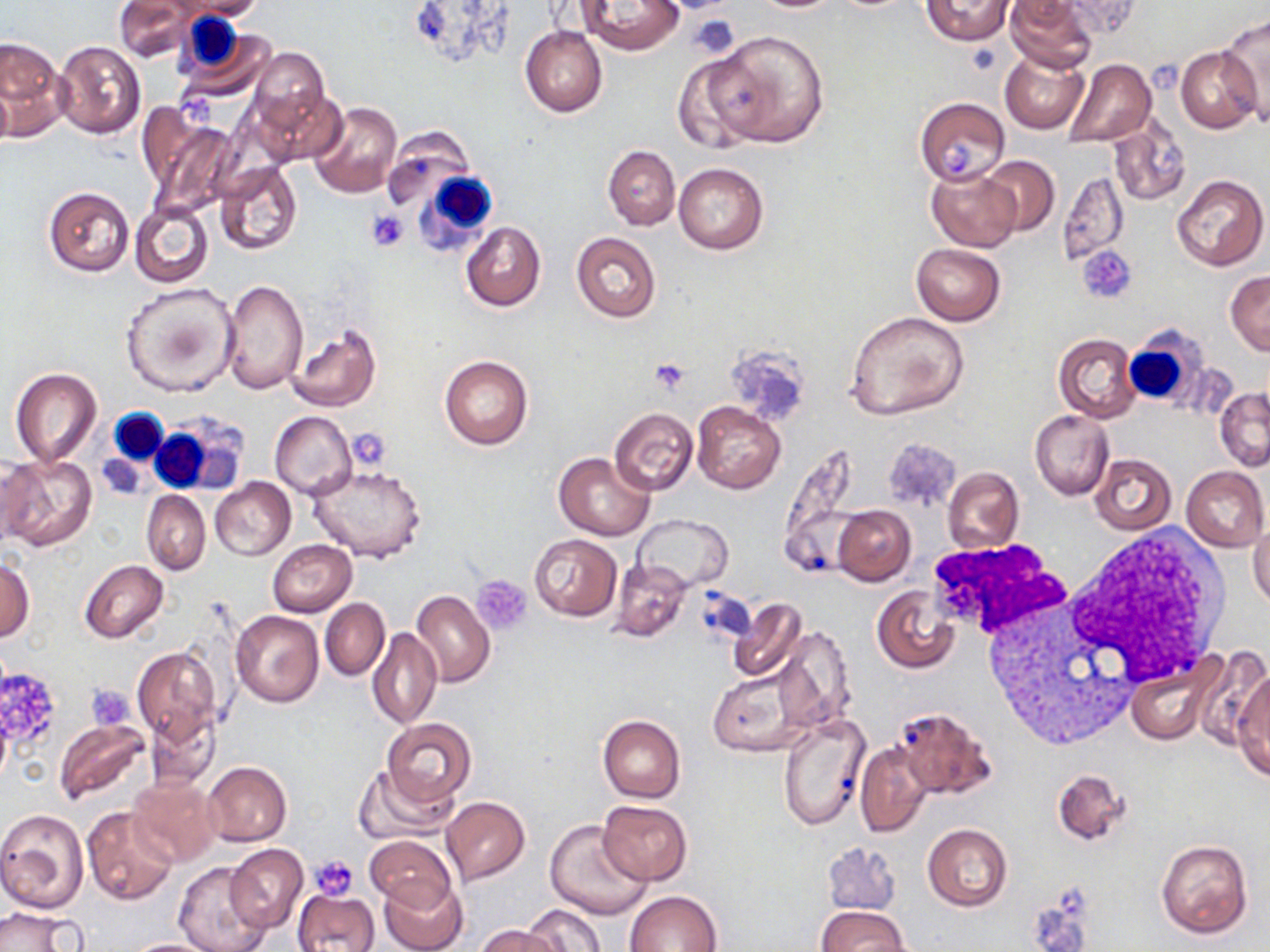 Approximate bounding boxes as (x1,y1)-(x2,y2) corner pairs in pixels. White blood cell locations: (175,10)-(245,77), (414,169)-(497,253), (1125,330)-(1205,409), (108,397)-(168,468), (151,413)-(245,499), (1064,528)-(1233,683), (934,549)-(1127,742). Platelet locations: (689,14)-(742,57), (1147,59)-(1178,93), (942,137)-(977,178), (367,210)-(409,252), (1079,247)-(1136,302), (650,358)-(693,394), (347,430)-(391,471), (473,575)-(532,635), (0,672)-(55,744), (85,683)-(135,731), (309,855)-(357,900). Uninfected red blood cell locations: (114,0)-(194,61), (169,0)-(266,21), (579,0)-(684,55), (920,0)-(1015,46), (1003,0)-(1097,74), (1057,0)-(1141,38), (1218,16)-(1270,125), (520,26)-(607,116), (179,27)-(277,104), (709,31)-(829,148), (1,36)-(67,139), (54,41)-(145,138), (1176,46)-(1262,133), (248,48)-(330,134), (1000,50)-(1087,135), (670,55)-(760,155), (1062,58)-(1155,147), (0,78)-(13,150), (255,86)-(346,167), (914,97)-(1011,185), (307,101)-(403,200), (142,108)-(238,214), (1109,118)-(1190,207), (379,127)-(477,216), (603,146)-(680,230), (979,154)-(1060,237), (214,160)-(302,256), (674,162)-(768,255), (925,165)-(1020,252), (1059,171)-(1129,265), (1170,175)-(1267,271), (42,186)-(135,277), (129,202)-(212,288), (461,221)-(545,310), (571,232)-(662,322), (910,243)-(1005,325), (1226,271)-(1270,354), (218,280)-(308,394), (121,282)-(239,397), (845,311)-(970,420), (286,324)-(382,412), (1054,332)-(1141,423), (439,354)-(533,450), (10,368)-(102,466), (1215,388)-(1270,471), (692,403)-(786,495), (609,407)-(699,497), (1030,409)-(1114,500), (270,411)-(355,500), (886,439)-(959,512), (546,451)-(643,621), (554,453)-(654,540), (2,454)-(97,552), (1090,454)-(1176,536), (306,463)-(427,562), (1181,465)-(1269,550), (943,466)-(1024,554), (209,477)-(295,560), (141,491)-(211,575), (833,506)-(915,585), (633,515)-(733,592), (1249,520)-(1270,610), (529,534)-(622,620), (267,539)-(357,617), (0,559)-(34,642), (80,560)-(167,643), (610,561)-(692,642), (871,585)-(961,673), (412,590)-(495,689), (320,598)-(389,680), (728,598)-(806,684), (230,610)-(325,707), (772,625)-(857,734), (367,629)-(441,730), (132,647)-(221,745), (1208,652)-(1270,762), (1125,653)-(1224,746), (706,663)-(816,758), (1233,671)-(1270,780), (892,706)-(996,799), (144,712)-(219,793), (598,714)-(685,802), (777,714)-(867,832), (382,718)-(476,805), (54,720)-(151,806), (855,744)-(932,838), (203,761)-(292,846), (355,764)-(454,844), (1052,768)-(1132,847), (128,777)-(220,867), (441,797)-(529,884), (598,801)-(693,885), (82,808)-(179,906), (0,810)-(88,913), (545,818)-(652,920), (922,824)-(1012,911), (364,836)-(455,911), (1155,840)-(1252,938), (224,844)-(307,933), (174,863)-(269,952), (379,875)-(469,952), (294,888)-(379,952), (625,890)-(722,951), (521,904)-(606,952), (816,905)-(906,952), (0,907)-(82,952), (475,925)-(562,952), (121,938)-(221,952). Slide-level diagnosis: negative for blood parasites. Image is 1270×952 pixels. Thin blood smear. May-Grünwald-Giemsa stain. Captured at 1000x magnification. Light microscopy. Single field of view.